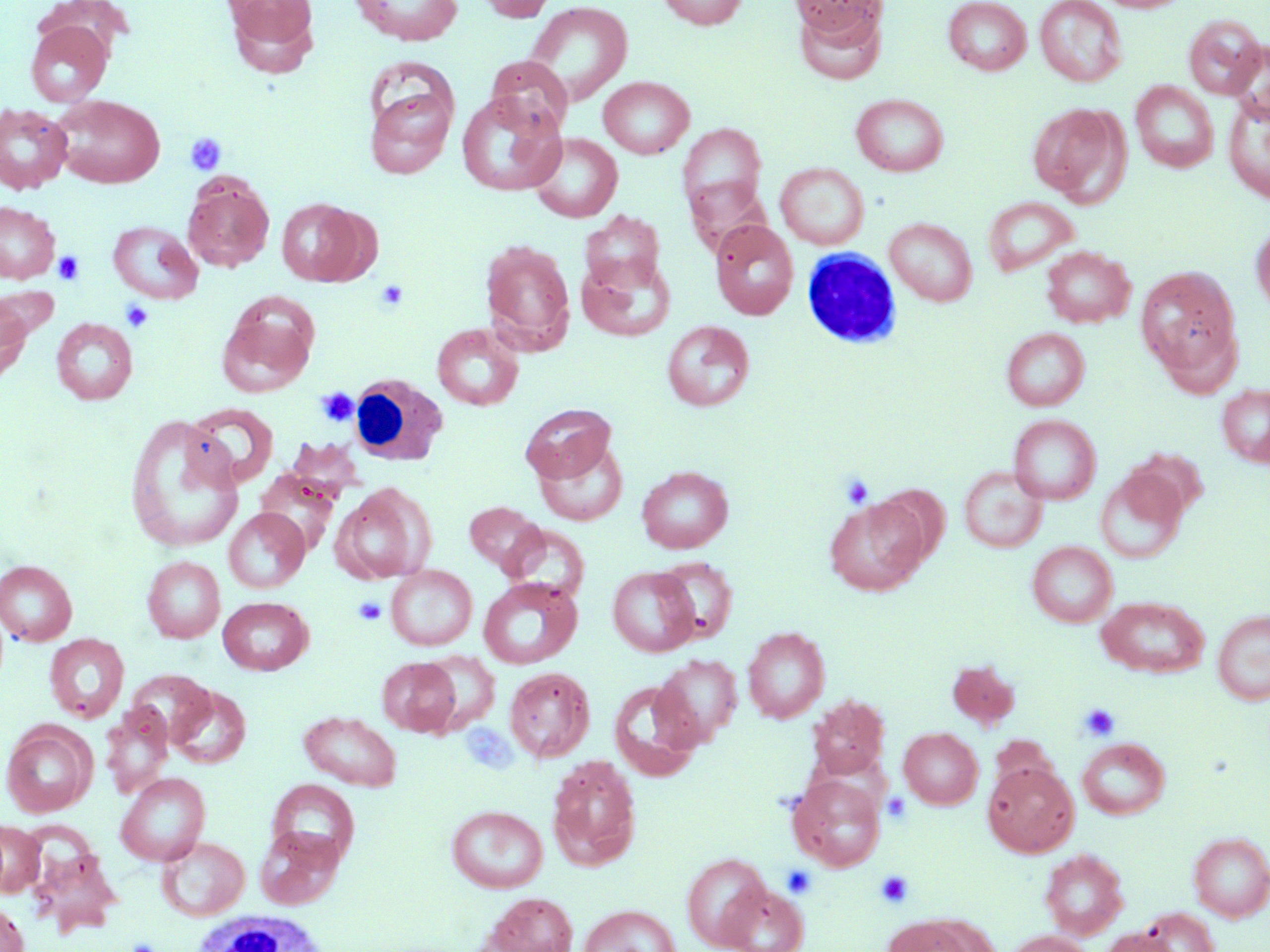
Approximate bounding boxes as named x1/y1/x2/y2 corners in pixels. Platelet locations: (x1=184, y1=132, x2=228, y2=176), (x1=52, y1=250, x2=86, y2=285), (x1=375, y1=279, x2=409, y2=312), (x1=121, y1=300, x2=154, y2=333), (x1=316, y1=387, x2=359, y2=427), (x1=840, y1=474, x2=874, y2=508), (x1=353, y1=596, x2=387, y2=626), (x1=1079, y1=703, x2=1120, y2=742), (x1=882, y1=792, x2=911, y2=823), (x1=781, y1=865, x2=818, y2=899), (x1=875, y1=869, x2=914, y2=909), (x1=126, y1=938, x2=160, y2=952). Uninfected red blood cell locations: (x1=222, y1=0, x2=321, y2=77), (x1=349, y1=0, x2=464, y2=45), (x1=471, y1=0, x2=561, y2=22), (x1=657, y1=0, x2=749, y2=30), (x1=792, y1=0, x2=884, y2=40), (x1=943, y1=0, x2=1032, y2=75), (x1=1094, y1=0, x2=1193, y2=13), (x1=523, y1=1, x2=634, y2=108), (x1=1035, y1=1, x2=1127, y2=87), (x1=795, y1=5, x2=887, y2=86), (x1=1183, y1=15, x2=1266, y2=99), (x1=25, y1=21, x2=113, y2=107), (x1=1229, y1=40, x2=1270, y2=123), (x1=485, y1=56, x2=573, y2=137), (x1=598, y1=76, x2=694, y2=159), (x1=1131, y1=81, x2=1218, y2=173), (x1=364, y1=85, x2=456, y2=179), (x1=456, y1=92, x2=566, y2=196), (x1=851, y1=93, x2=949, y2=176), (x1=52, y1=95, x2=166, y2=188), (x1=1223, y1=98, x2=1270, y2=203), (x1=1027, y1=103, x2=1127, y2=203), (x1=0, y1=105, x2=72, y2=193), (x1=677, y1=123, x2=766, y2=218), (x1=527, y1=133, x2=623, y2=223), (x1=775, y1=162, x2=869, y2=249), (x1=183, y1=176, x2=274, y2=272), (x1=685, y1=177, x2=770, y2=257), (x1=983, y1=197, x2=1080, y2=276), (x1=275, y1=198, x2=367, y2=286), (x1=0, y1=202, x2=59, y2=283), (x1=580, y1=211, x2=665, y2=295), (x1=885, y1=218, x2=978, y2=306), (x1=709, y1=219, x2=798, y2=320), (x1=1251, y1=219, x2=1270, y2=316), (x1=108, y1=221, x2=203, y2=303), (x1=480, y1=239, x2=575, y2=353), (x1=1041, y1=246, x2=1135, y2=328), (x1=576, y1=252, x2=675, y2=343), (x1=1136, y1=265, x2=1243, y2=383), (x1=0, y1=292, x2=33, y2=387), (x1=217, y1=305, x2=317, y2=398), (x1=51, y1=318, x2=138, y2=404), (x1=662, y1=320, x2=755, y2=412), (x1=432, y1=324, x2=524, y2=410), (x1=1001, y1=327, x2=1089, y2=411), (x1=1217, y1=385, x2=1270, y2=467), (x1=185, y1=402, x2=279, y2=489), (x1=520, y1=403, x2=616, y2=484), (x1=124, y1=413, x2=244, y2=554), (x1=1009, y1=414, x2=1101, y2=505), (x1=534, y1=438, x2=628, y2=526), (x1=1126, y1=447, x2=1209, y2=520), (x1=637, y1=465, x2=733, y2=553), (x1=959, y1=466, x2=1047, y2=552), (x1=255, y1=468, x2=341, y2=557), (x1=1095, y1=469, x2=1186, y2=564), (x1=331, y1=485, x2=434, y2=584), (x1=824, y1=498, x2=929, y2=596), (x1=464, y1=501, x2=547, y2=576), (x1=223, y1=508, x2=309, y2=593), (x1=502, y1=524, x2=590, y2=602), (x1=1027, y1=542, x2=1117, y2=627), (x1=142, y1=556, x2=225, y2=643), (x1=653, y1=556, x2=738, y2=643), (x1=1, y1=560, x2=78, y2=645), (x1=386, y1=565, x2=477, y2=651), (x1=607, y1=566, x2=699, y2=657), (x1=478, y1=577, x2=582, y2=669), (x1=1096, y1=595, x2=1210, y2=678), (x1=218, y1=597, x2=313, y2=675), (x1=1213, y1=610, x2=1270, y2=705), (x1=743, y1=627, x2=829, y2=723), (x1=44, y1=634, x2=129, y2=723), (x1=421, y1=650, x2=500, y2=732), (x1=654, y1=654, x2=743, y2=746), (x1=377, y1=657, x2=461, y2=736), (x1=947, y1=660, x2=1019, y2=728), (x1=504, y1=666, x2=595, y2=762), (x1=125, y1=668, x2=214, y2=747), (x1=502, y1=672, x2=693, y2=767), (x1=609, y1=679, x2=704, y2=782), (x1=168, y1=685, x2=251, y2=768), (x1=808, y1=694, x2=889, y2=779), (x1=100, y1=703, x2=174, y2=798), (x1=299, y1=711, x2=402, y2=791), (x1=1, y1=722, x2=96, y2=817), (x1=899, y1=727, x2=983, y2=809), (x1=1078, y1=738, x2=1170, y2=820), (x1=547, y1=754, x2=641, y2=870), (x1=983, y1=762, x2=1078, y2=857), (x1=115, y1=772, x2=210, y2=866), (x1=787, y1=773, x2=886, y2=872), (x1=267, y1=779, x2=360, y2=866), (x1=447, y1=805, x2=548, y2=893), (x1=0, y1=821, x2=44, y2=897), (x1=255, y1=825, x2=344, y2=910), (x1=1188, y1=832, x2=1270, y2=921), (x1=157, y1=836, x2=250, y2=921), (x1=26, y1=840, x2=122, y2=935), (x1=1040, y1=848, x2=1128, y2=939), (x1=681, y1=852, x2=772, y2=950), (x1=720, y1=883, x2=809, y2=951), (x1=483, y1=893, x2=579, y2=951), (x1=0, y1=902, x2=29, y2=952), (x1=578, y1=904, x2=682, y2=952), (x1=1139, y1=907, x2=1220, y2=952), (x1=881, y1=914, x2=988, y2=952), (x1=1100, y1=927, x2=1180, y2=952), (x1=1002, y1=930, x2=1095, y2=952). White blood cell locations: (x1=801, y1=248, x2=902, y2=350), (x1=347, y1=375, x2=447, y2=466), (x1=195, y1=911, x2=329, y2=952). Slide-level diagnosis: negative for blood parasites. May-Grünwald-Giemsa-stained preparation. Thin blood smear. Image is 1270×952 pixels. Captured at 1000x magnification. One field of a larger specimen. Optical microscopy.